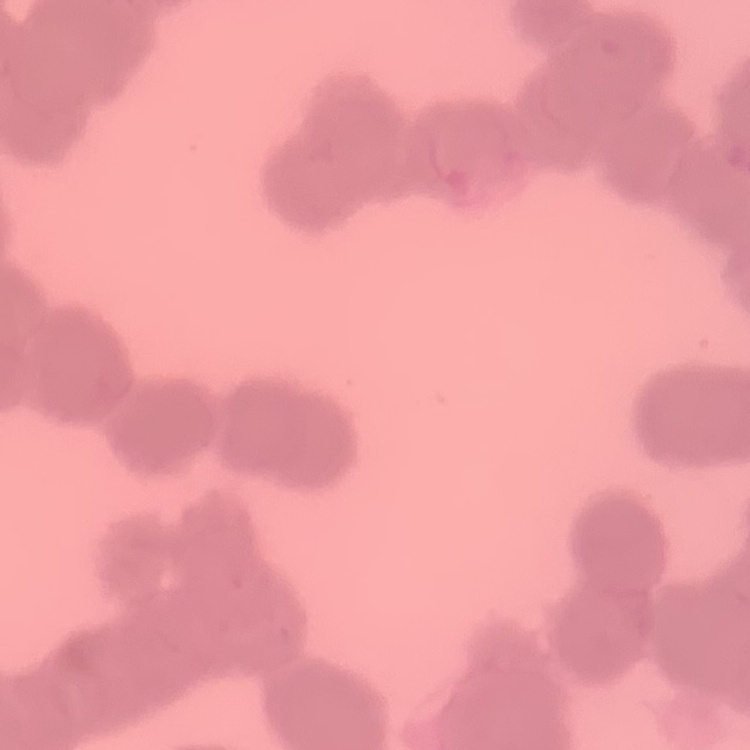

{
  "erythrocyte_morphology": "rouleaux formation",
  "preparation": "thin peripheral smear",
  "image_type": "one tile cut from a larger photomicrograph",
  "stain": "Field's or Giemsa"
}